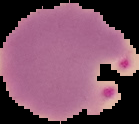
Summary:
  - Image size: 139×124 pixels
  - Preparation: thin blood film
  - Result: Plasmodium parasites detected
  - Image type: segmented cell region with the area outside set to black